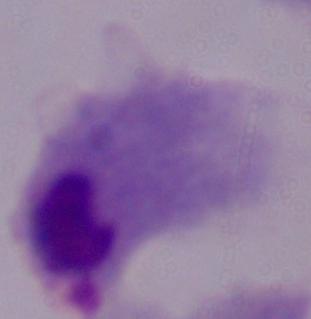
magnification = 1000x
modality = micrograph
identification = trichomonad